Assess this cell for malaria.
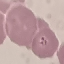
Parasitized.

{
  "stain": "Giemsa",
  "capture": "smartphone camera at the microscope eyepiece",
  "preparation": "thin blood film",
  "image_type": "cell patch, automatically extracted from a larger field of view and resized to 64 × 64 pixels"
}